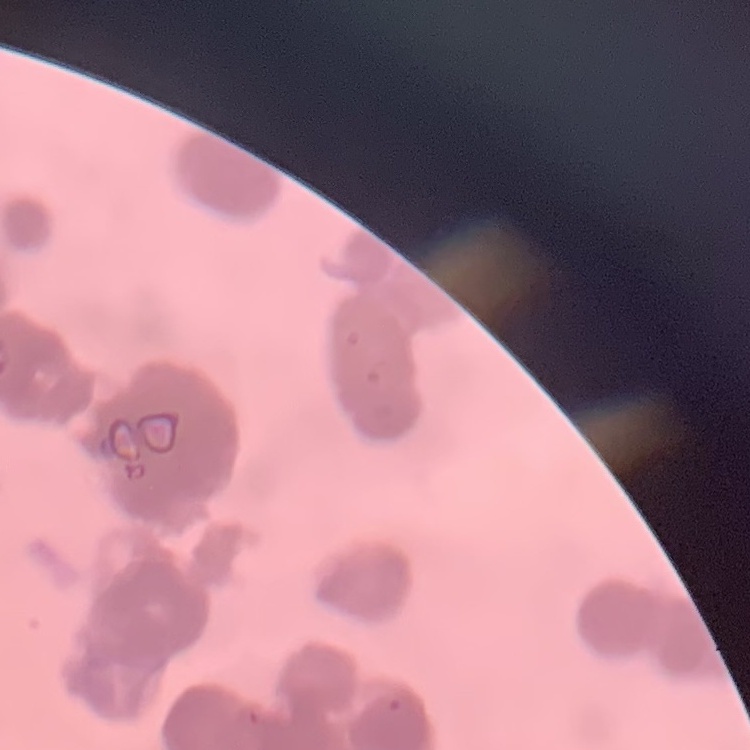
red blood cell morphology = rouleaux formation
stain = Field's or Giemsa
preparation = thin blood film
image type = one tile cut from a larger photomicrograph